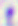

Summary:
  - Identification: Toxoplasma gondii
  - Magnification: 400x
  - Modality: photomicrograph